Classify this cell by malaria status.
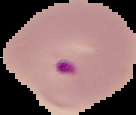

It is parasitized.

{
  "image_size": "136×115 pixels",
  "image_type": "segmented cell region on a black background",
  "preparation": "thin blood smear"
}